Classify this cell by malaria status.
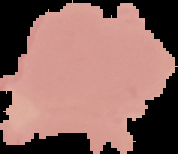
It is uninfected.

Image is 178×154 pixels. Cell region segmented out of the field of view; the surrounding area is masked to black. From a thin blood film.